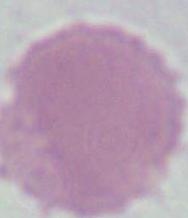

Captured at 1000x magnification. An erythrocyte is shown. Photomicrograph.